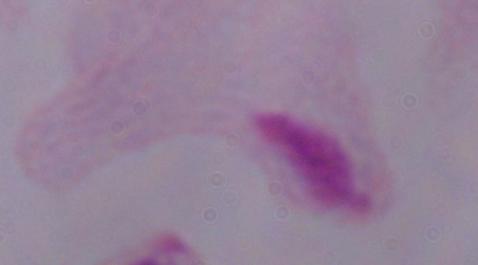

Summary:
  - Magnification: 1000x
  - Modality: photomicrograph
  - Identification: trichomonad